Assess this cell for malaria.
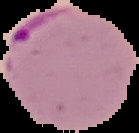
It is parasitized.

image size = 139×133 pixels
image type = segmented cell region with the area outside set to black
preparation = thin blood film